Identify the parasite.
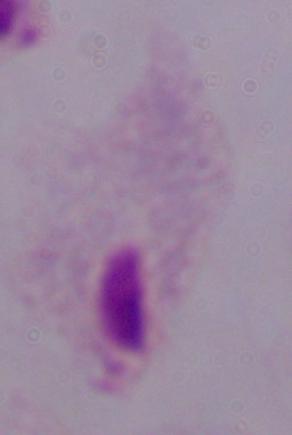
A trichomonad.

magnification = 1000x
modality = micrograph